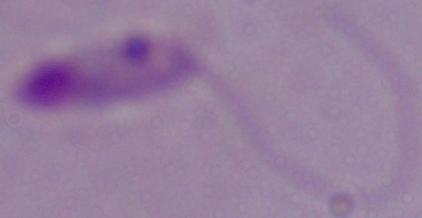
modality: micrograph
identification: Leishmania
magnification: 1000x